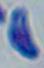

magnification = 1000x
modality = photomicrograph
identification = Toxoplasma gondii